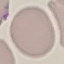

Summary:
  - Result: negative for malaria parasites
  - Stain: Giemsa
  - Image type: automatically extracted cell patch, resized to 64 × 64 pixels
  - Preparation: thin smear
  - Capture: smartphone camera at the microscope eyepiece